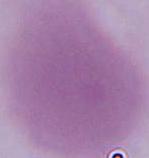
Summary:
  - Magnification: 1000x
  - Modality: photomicrograph
  - Identification: red blood cell